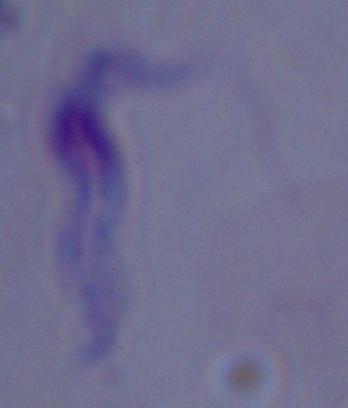

identification = trypanosome
magnification = 1000x
modality = micrograph